Classify this cell by malaria status.
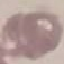
It is uninfected.

image type = automatically extracted cell patch, resized to 64 × 64 pixels
capture = smartphone camera at the microscope eyepiece
preparation = thin smear
stain = Giemsa